Name the parasite shown.
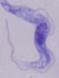
A trypanosome.

Summary:
  - Magnification: 1000x
  - Modality: photomicrograph